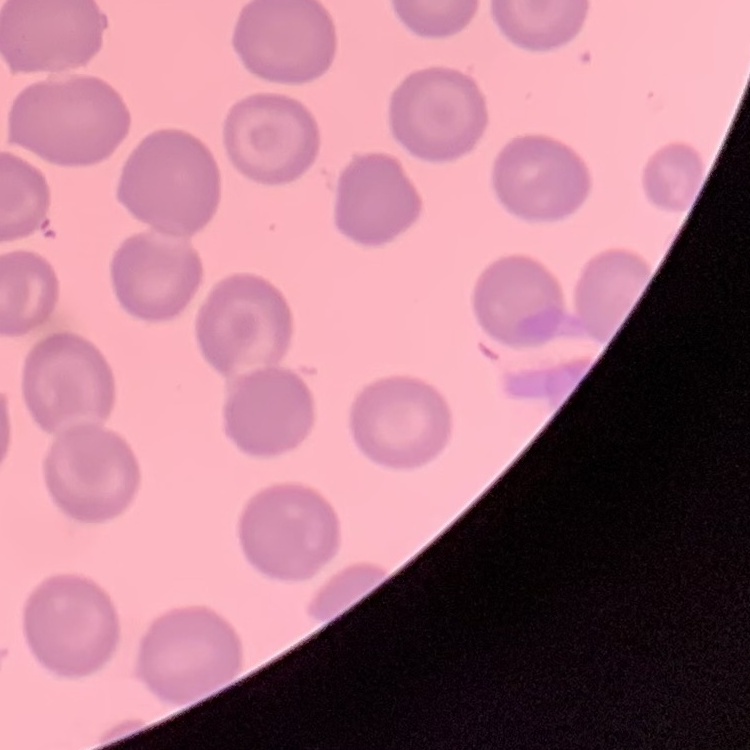
red blood cell morphology = no rouleaux formation
preparation = thin peripheral smear
stain = Field's or Giemsa
image type = one tile cut from a larger photomicrograph